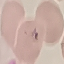
result = malaria parasites detected
capture = smartphone camera at the microscope eyepiece
preparation = thin blood smear
stain = Giemsa
image type = cell patch, automatically extracted from a larger field of view and resized to 64 × 64 pixels